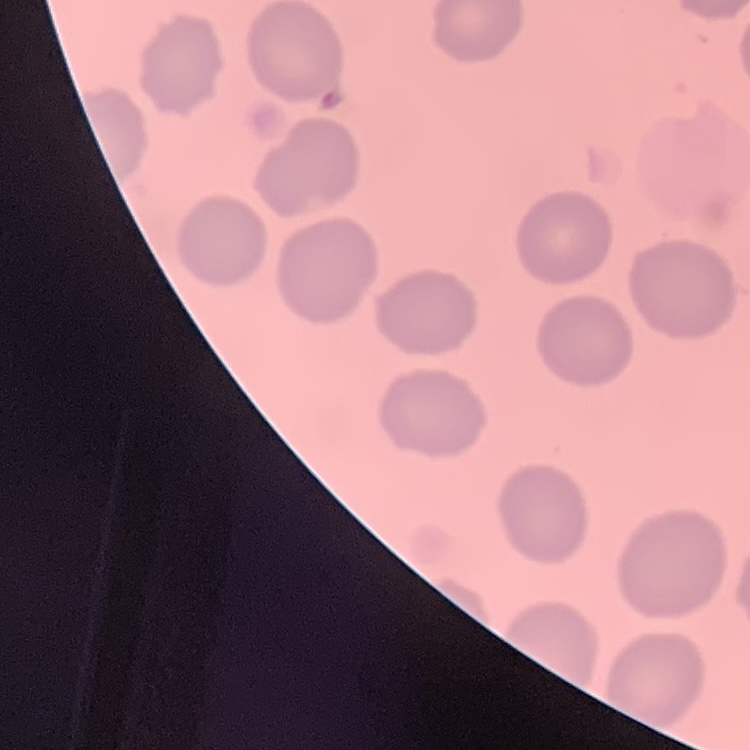

The erythrocytes exhibit no rouleaux formation. Field's or Giemsa stain. One tile cut from a larger photomicrograph. Thin blood film.